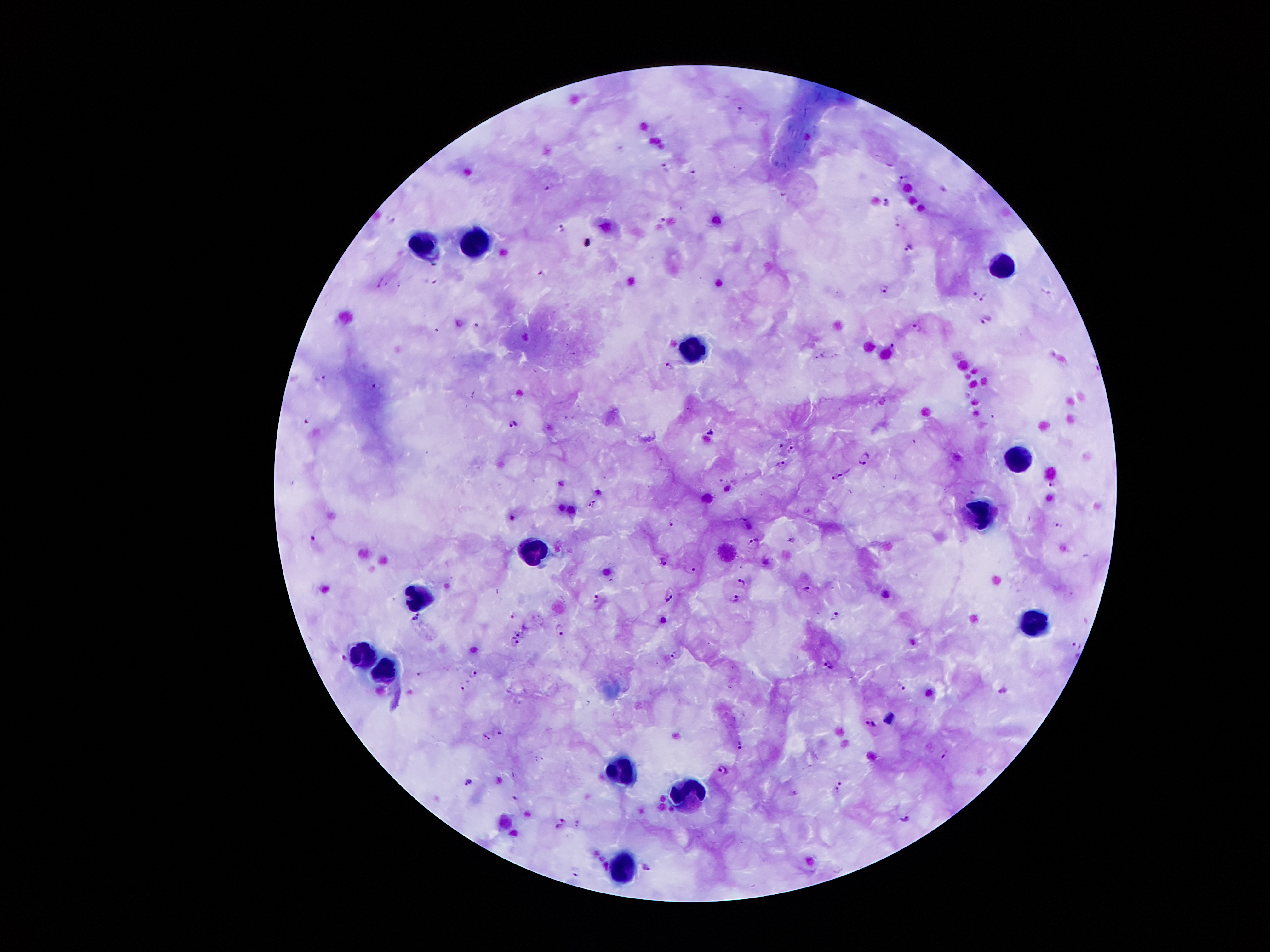
Approximate object centers, in pixels from the top-left corner. Plasmodium parasite locations: (x=739, y=109), (x=665, y=167), (x=694, y=172), (x=905, y=178), (x=549, y=185), (x=888, y=202), (x=898, y=221), (x=563, y=227), (x=912, y=247), (x=884, y=288), (x=972, y=293), (x=983, y=298), (x=986, y=319), (x=917, y=326), (x=894, y=345), (x=668, y=366), (x=321, y=378), (x=375, y=386), (x=309, y=419), (x=513, y=424), (x=708, y=432), (x=782, y=446), (x=791, y=449), (x=864, y=458), (x=783, y=463), (x=839, y=475), (x=1052, y=484), (x=592, y=504), (x=673, y=521), (x=1056, y=523), (x=753, y=543), (x=664, y=561), (x=691, y=569), (x=740, y=582), (x=806, y=589), (x=670, y=595), (x=735, y=596), (x=597, y=598), (x=513, y=614), (x=417, y=615), (x=835, y=615), (x=559, y=628), (x=519, y=633), (x=515, y=642), (x=1078, y=645), (x=674, y=654), (x=344, y=659), (x=830, y=664), (x=472, y=673), (x=464, y=686), (x=901, y=687), (x=1004, y=691), (x=869, y=724), (x=498, y=731), (x=487, y=736), (x=738, y=744), (x=944, y=754), (x=725, y=768), (x=469, y=782), (x=837, y=786), (x=793, y=793), (x=563, y=819), (x=905, y=819), (x=646, y=868). Leukocyte locations: (x=425, y=243), (x=473, y=243), (x=1002, y=263), (x=690, y=348), (x=1022, y=460), (x=985, y=514), (x=530, y=548), (x=420, y=597), (x=1029, y=624), (x=361, y=661), (x=381, y=670), (x=617, y=768), (x=688, y=794), (x=618, y=869). Smartphone photograph taken through the microscope eyepiece. Patient malaria status: infected with Plasmodium falciparum. 100x magnification. Giemsa stain. Single field of view. Thick blood smear. Image is 1270×952 pixels.